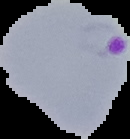

image size = 130×139 pixels
malaria status = parasitized
image type = segmented cell region on a black background
preparation = thin blood smear